Locate the red blood cells and classify each one as P. falciparum-infected, uninfected, or of indeterminate infection status.
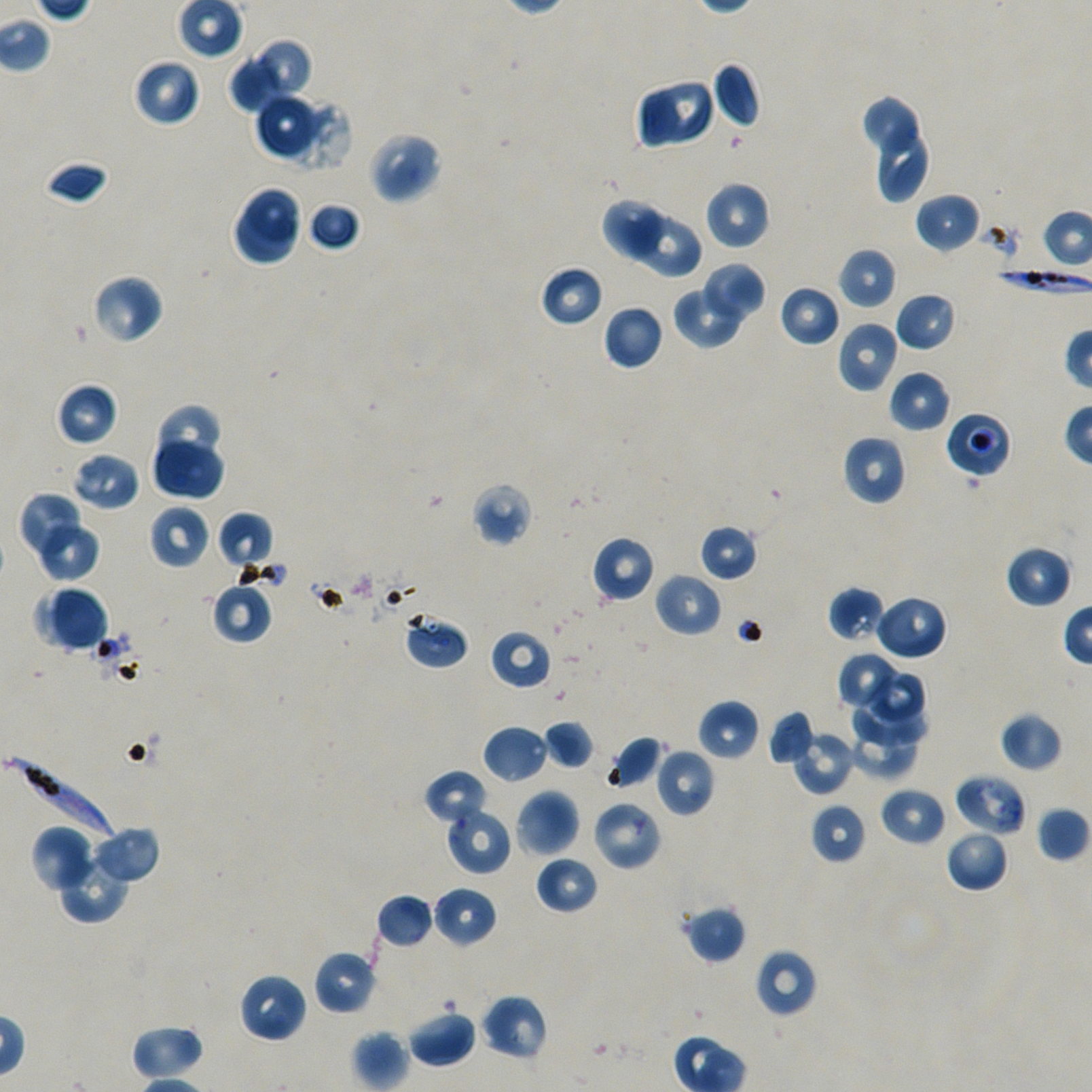

Approximate bounding boxes as (x1, y1, x2, y2) in pixels. Not every red blood cell is marked.
Infected red blood cells: (976, 259, 1092, 306), (4, 755, 114, 841).
Red blood cells of indeterminate infection status: (945, 411, 1011, 479), (401, 611, 471, 670), (955, 773, 1027, 837).
Uninfected red blood cells: (257, 37, 310, 99), (228, 55, 283, 117), (132, 57, 201, 127), (711, 62, 762, 129), (652, 79, 712, 145), (635, 83, 682, 150), (254, 92, 318, 156), (862, 96, 917, 154), (273, 97, 351, 173), (879, 126, 928, 202), (367, 131, 443, 204), (44, 160, 110, 206), (704, 181, 771, 251), (243, 185, 304, 244), (915, 192, 981, 254), (230, 200, 298, 270), (307, 200, 361, 252), (602, 200, 663, 263), (632, 212, 700, 276), (838, 247, 898, 309), (702, 263, 767, 323), (539, 265, 604, 328), (92, 274, 164, 345), (778, 284, 840, 348), (672, 285, 747, 349), (894, 291, 958, 352), (602, 304, 663, 371), (836, 320, 900, 393), (888, 369, 951, 433), (56, 382, 117, 446), (152, 404, 227, 471), (841, 435, 907, 506), (151, 438, 225, 500), (73, 452, 139, 510), (471, 481, 533, 547), (16, 490, 81, 557), (148, 504, 211, 570), (217, 511, 274, 571), (38, 522, 101, 583), (699, 524, 759, 582), (591, 535, 655, 604), (1004, 545, 1073, 608), (655, 571, 723, 638), (211, 581, 274, 644), (829, 585, 886, 644), (33, 586, 109, 653), (872, 593, 948, 661), (489, 629, 552, 691), (836, 652, 903, 712), (869, 672, 927, 725), (852, 691, 930, 746), (698, 698, 761, 761), (767, 710, 816, 766), (998, 711, 1063, 771), (541, 719, 595, 770), (848, 723, 916, 779), (481, 724, 549, 784), (790, 730, 856, 795), (606, 735, 664, 792), (654, 747, 715, 817), (424, 769, 488, 826), (879, 786, 947, 847), (514, 789, 580, 858), (591, 799, 662, 871), (444, 803, 512, 876), (809, 803, 868, 865), (1036, 806, 1089, 862), (90, 824, 161, 886), (30, 825, 98, 893), (945, 829, 1009, 893), (56, 853, 130, 924), (534, 854, 598, 915), (431, 885, 498, 948), (375, 894, 435, 948), (683, 904, 746, 964), (754, 948, 818, 1018), (312, 949, 377, 1015), (238, 972, 308, 1044), (480, 993, 549, 1061), (407, 1008, 477, 1068), (130, 1023, 204, 1080), (351, 1029, 410, 1091).

Summary:
  - Culture: static in-vitro P. falciparum strain NF54
  - Objective: 100x, oil immersion, numerical aperture 1.45
  - Image size: 1092×1092 pixels
  - Preparation: thin blood film
  - Field of view: single
  - Donor blood group: A+/O+
  - Stain: Giemsa